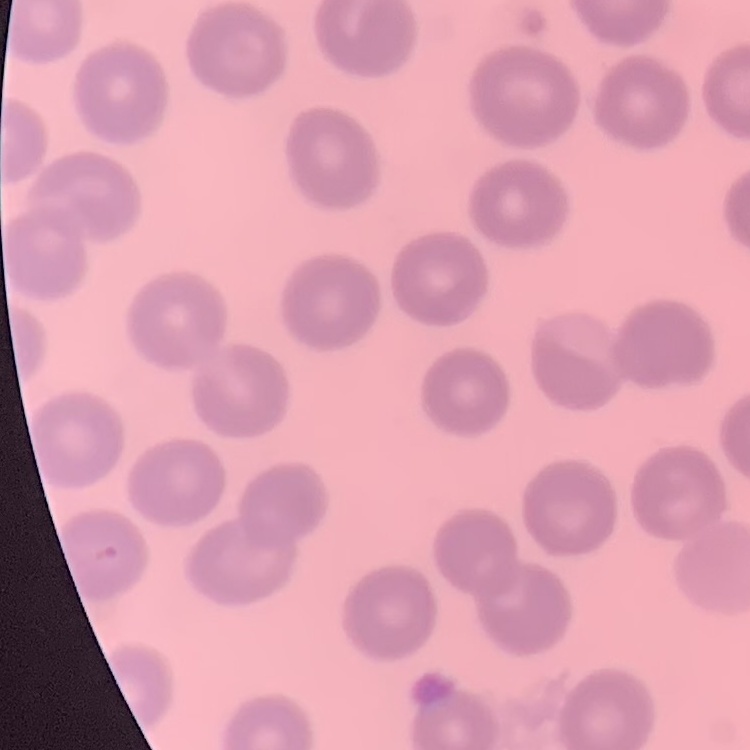 The erythrocytes show no rouleaux formation. Thin blood smear. Stained with either Field's or Giemsa. One tile cut from a larger photomicrograph.